Assess the morphology of the erythrocytes.
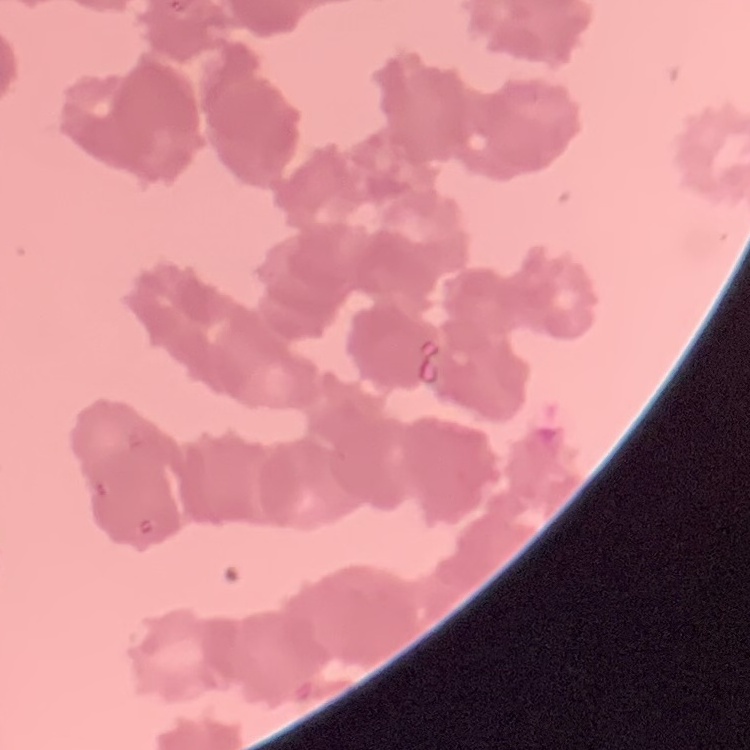
Rouleaux formation.

preparation = thin blood film
stain = Field's or Giemsa
image type = square crop of a larger photomicrograph